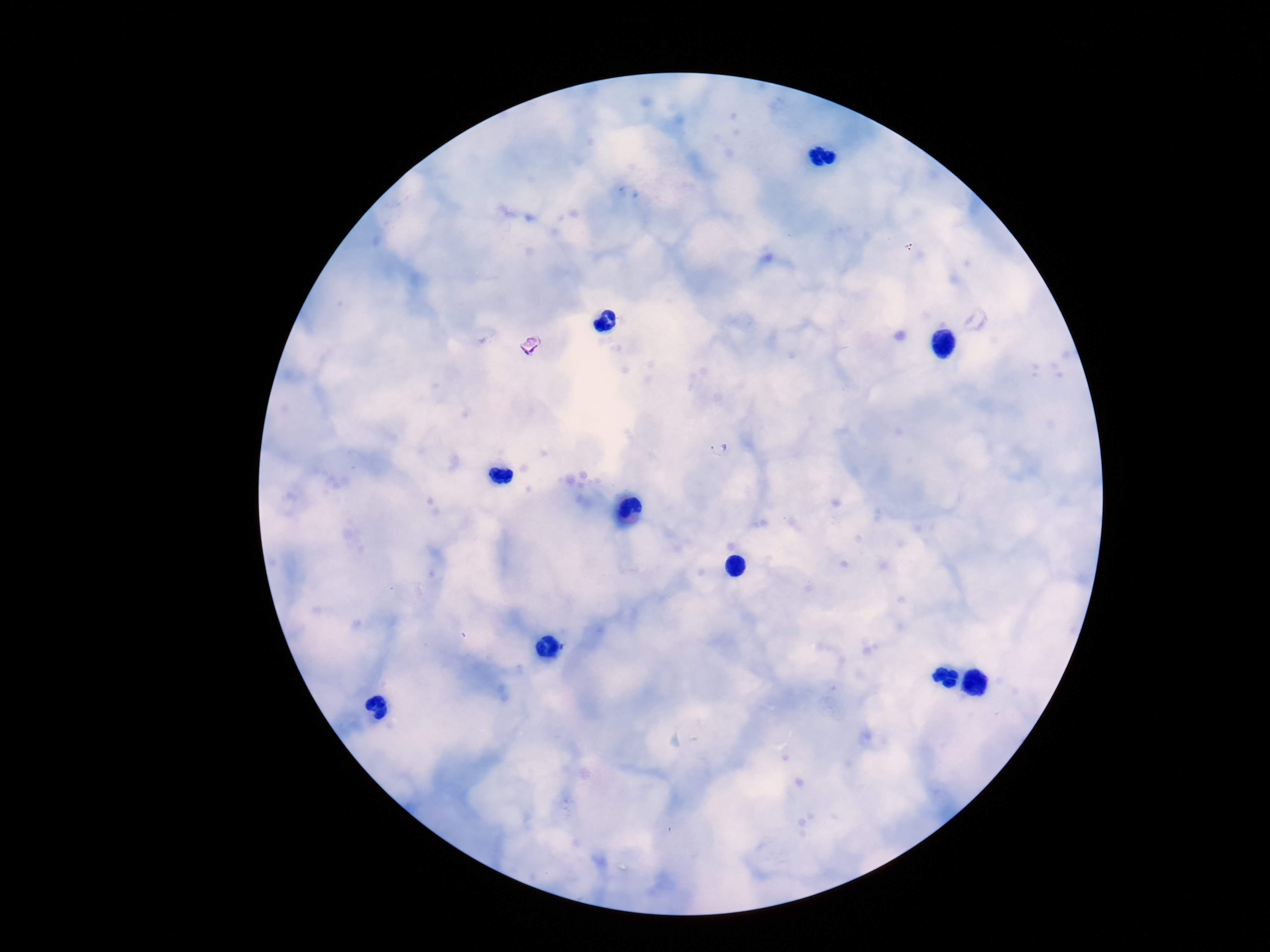
Approximate centers as {x, y} in pixels. Plasmodium parasite locations: {529, 343}, {718, 448}. Photographed through the microscope eyepiece with a smartphone camera. One field from this slide. Giemsa-stained preparation. Thick blood smear. Image is 1270×952 pixels. 100x magnification. Patient malaria status: infected.